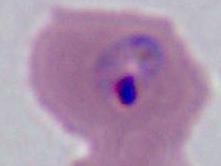

A Plasmodium parasite is seen. Photomicrograph. Captured at either 400x or 1000x magnification.